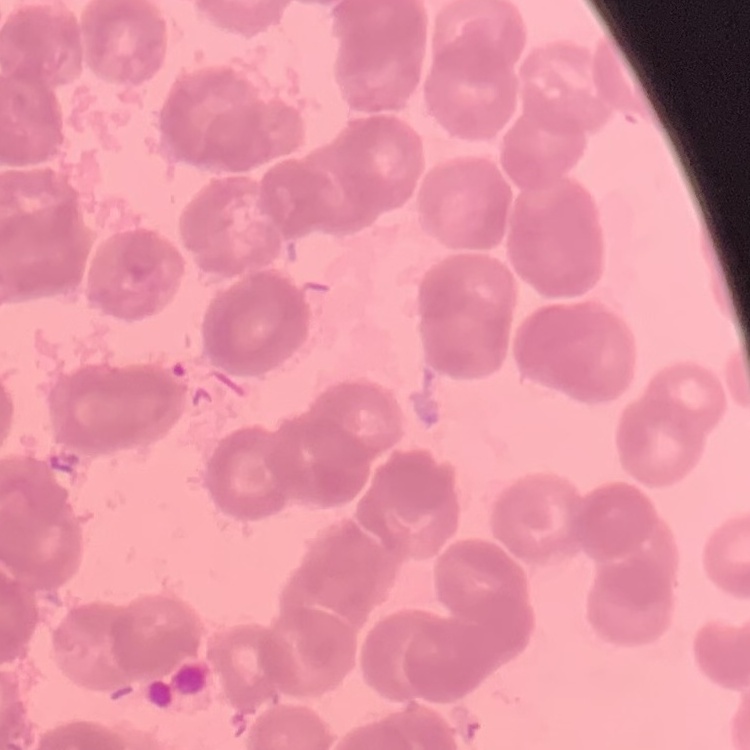

Summary:
  - Erythrocyte morphology: rouleaux formation
  - Preparation: thin blood smear
  - Image type: one tile cut from a larger photomicrograph
  - Stain: Field's or Giemsa